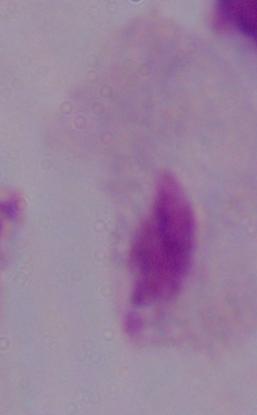

Summary:
  - Magnification: 1000x
  - Identification: trichomonad
  - Modality: micrograph